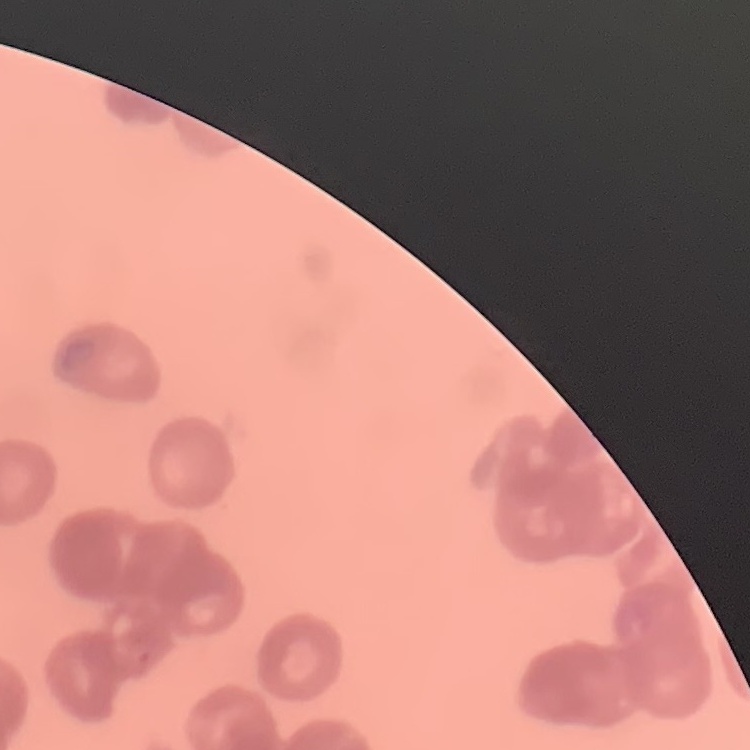

Summary:
  - Red blood cell morphology: rouleaux formation
  - Image type: one tile cut from a larger photomicrograph
  - Preparation: thin blood film
  - Stain: Field's or Giemsa